Identify the parasite.
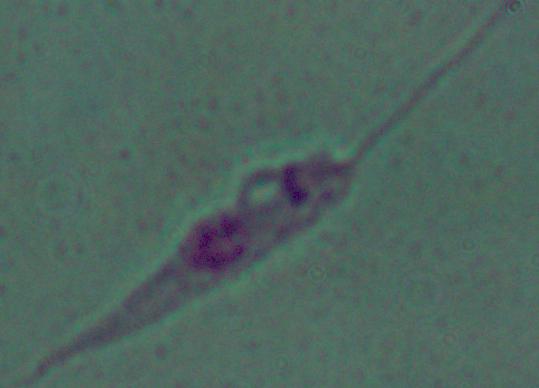
This is Leishmania.

magnification = 1000x
modality = micrograph